Point out each Plasmodium parasite.
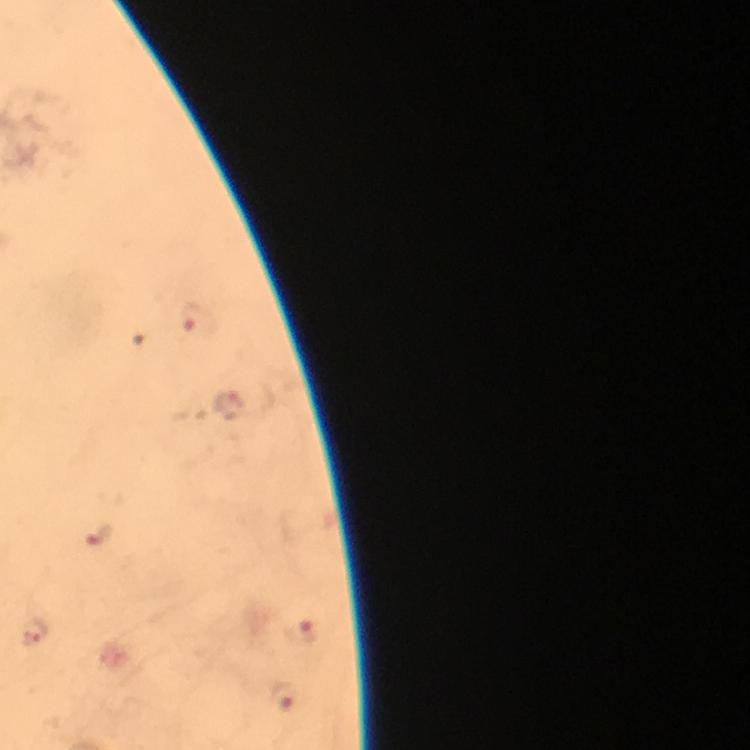

Approximate object centers, in pixels from the top-left corner.
Plasmodium parasites: (x=193, y=319), (x=233, y=408), (x=99, y=535), (x=37, y=631), (x=301, y=634), (x=284, y=698).

Summary:
  - Immersion oil: applied
  - Preparation: thick blood film
  - Image size: 750×750 pixels
  - Stain: Giemsa
  - Magnification: 100x
  - Context: from a malaria diagnostic workup
  - Capture: smartphone mounted on the microscope
  - Cropped from: a single field of view